Identify the preparation type.
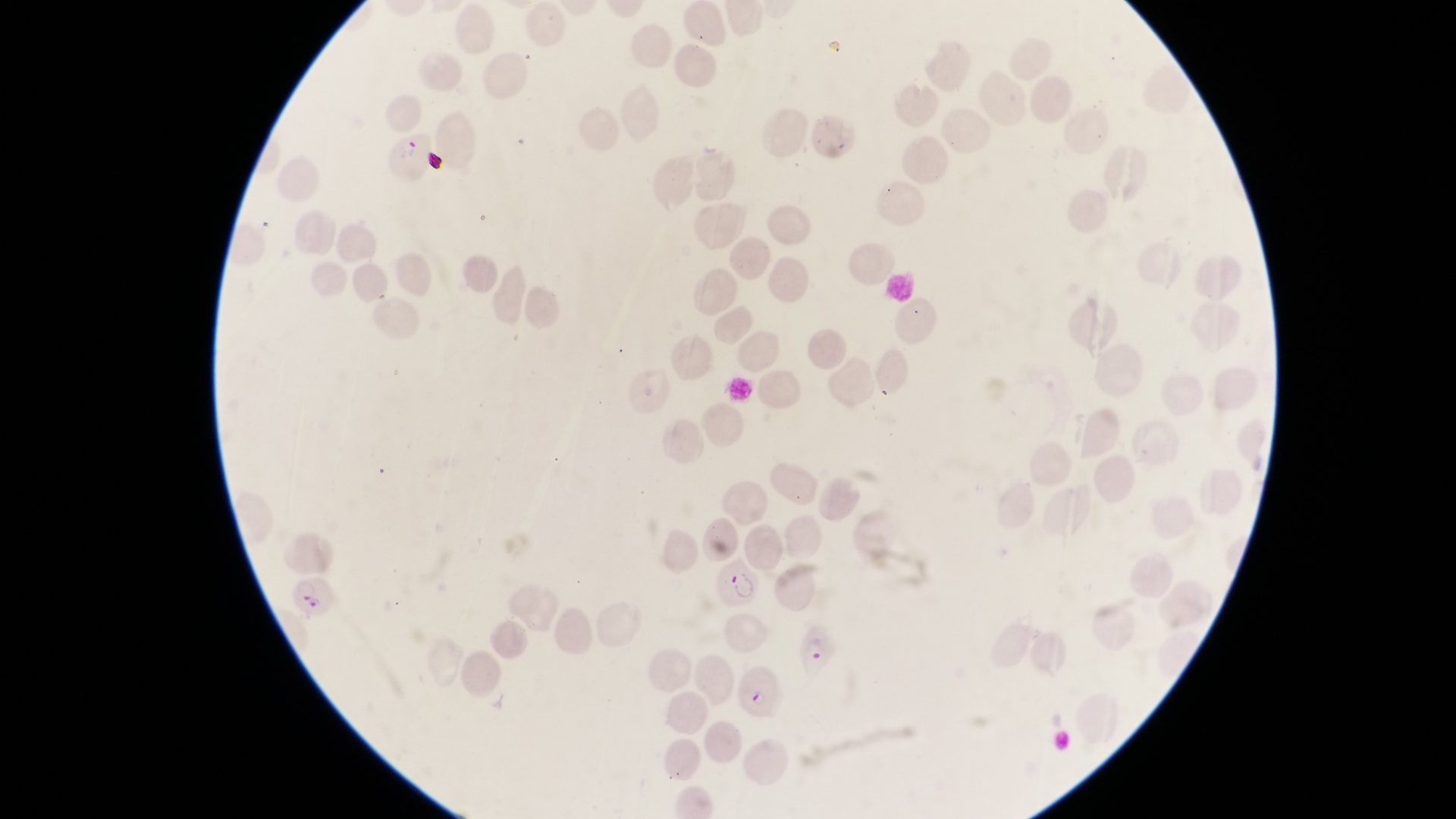

This is a thin smear.

Approximate bounding boxes as [left, top, right, bottom] in pixels. Parasitised red blood cell locations: [381, 130, 427, 183], [713, 558, 763, 616], [792, 624, 837, 677], [739, 661, 788, 722]. Artifact (platelet-like body, stain precipitate, or debris) locations: [419, 142, 446, 175]. Collected in Uganda. At a magnification of 1000x. Image is 1456×819 pixels. Photographed through the eyepiece of an Olympus CX-23 microscope with a smartphone camera. Single field of view.